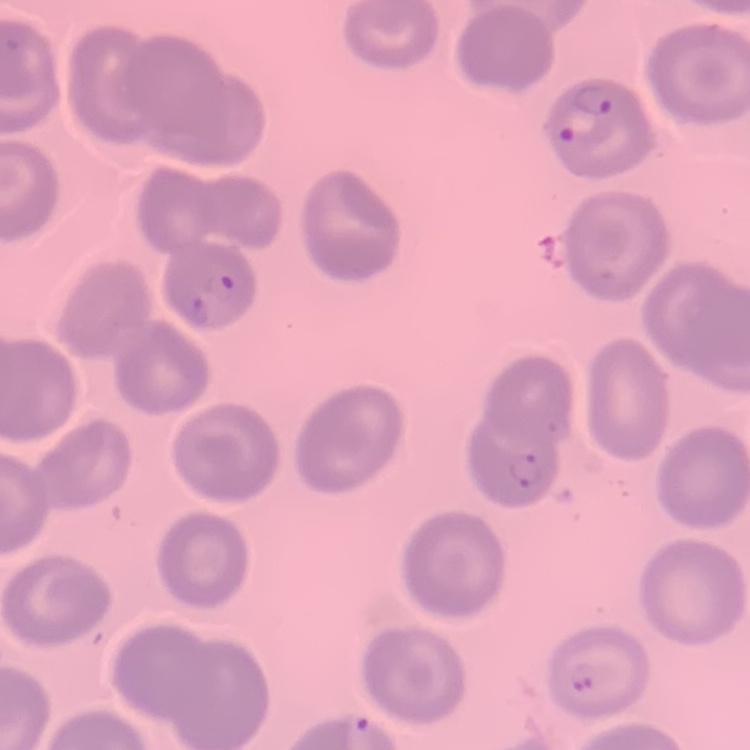

erythrocyte morphology = no rouleaux formation
preparation = thin blood film
stain = Field's or Giemsa
image type = square crop of a larger photomicrograph